Identify the parasite.
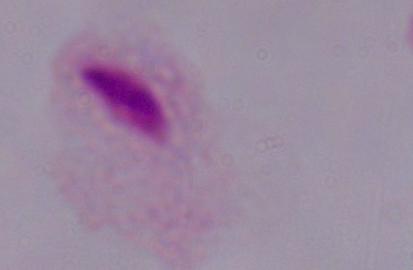
A trichomonad.

Captured at 1000x magnification. Micrograph.